Point out Plasmodium parasites and leukocytes.
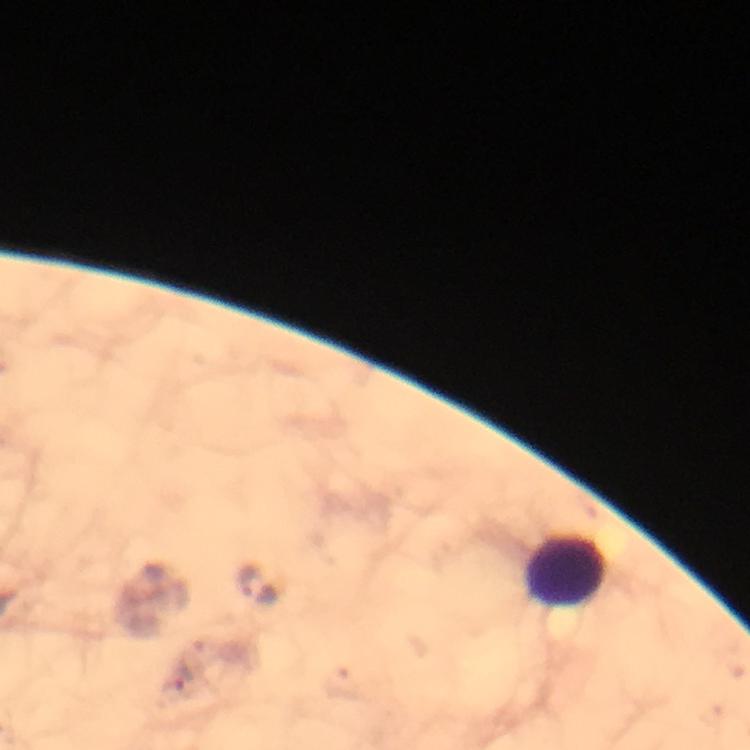

Approximate object centers, in pixels from the top-left corner.
Plasmodium parasites: (x=176, y=680).
Leukocytes: (x=565, y=571).

context = from a malaria diagnostic workup
magnification = 100x
preparation = thick smear
capture = smartphone photograph through a microscope
cropped from = one field of view
image size = 750×750 pixels
immersion oil = applied
stain = Giemsa